Report the malaria status of this cell.
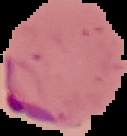

Parasitized.

image size = 127×136 pixels
image type = segmented cell region on a black background
preparation = thin blood smear